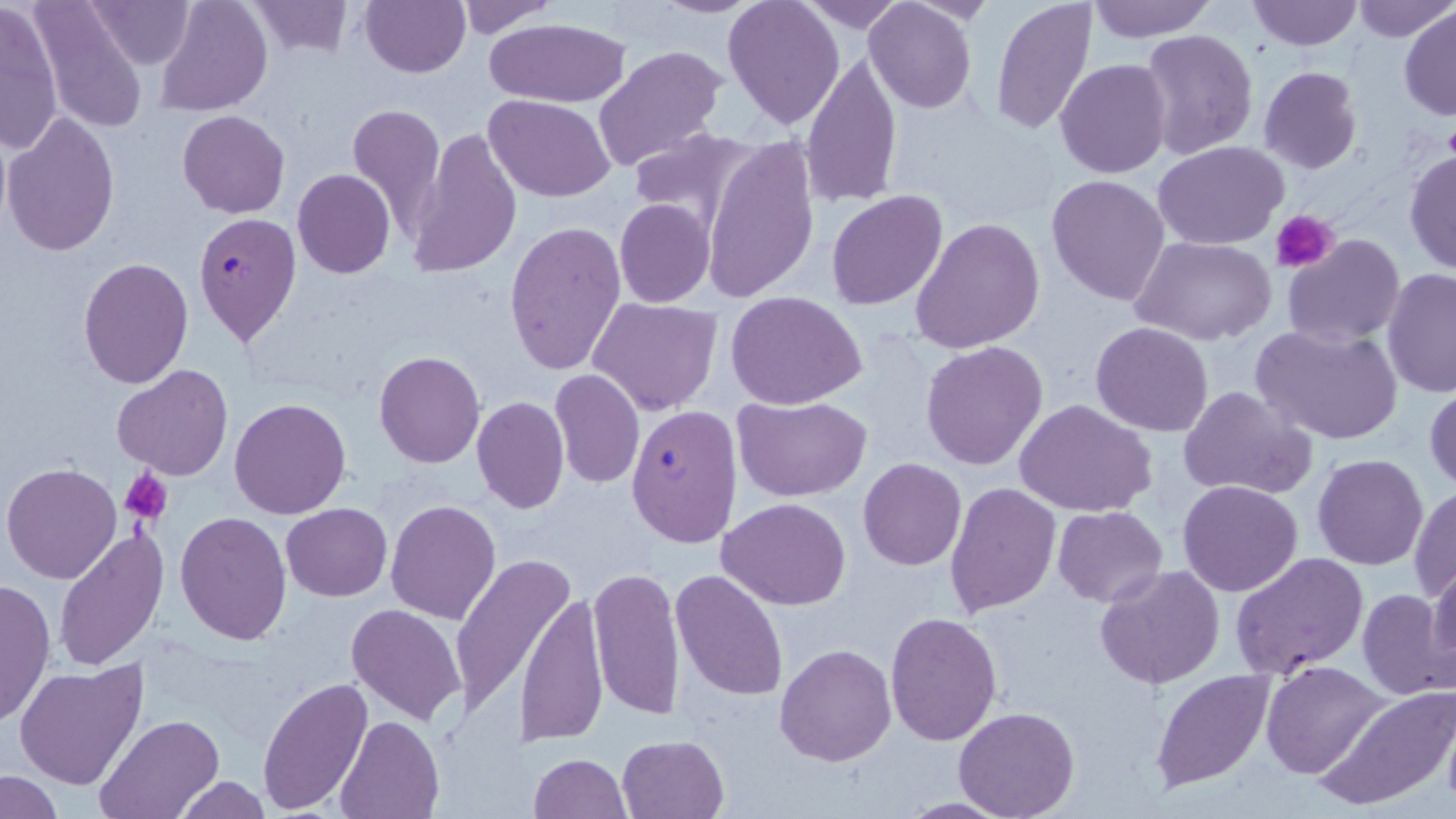

{
  "plasmodium_falciparum_infected_red_blood_cell_locations": "approximate bounding boxes as (x1, y1, x2, y2) in pixels: (195, 211, 302, 344), (625, 404, 742, 548)",
  "slide_level_diagnosis": "Plasmodium falciparum",
  "platelet_locations": "approximate bounding boxes as (x1, y1, x2, y2) in pixels: (1273, 210, 1340, 271), (120, 469, 172, 526)",
  "uninfected_red_blood_cell_locations": "approximate bounding boxes as (x1, y1, x2, y2) in pixels: (29, 0, 150, 135), (86, 0, 197, 70), (155, 0, 273, 117), (358, 0, 471, 78), (452, 0, 564, 37), (648, 0, 767, 18), (723, 0, 846, 129), (801, 0, 906, 33), (1247, 0, 1362, 50), (1350, 0, 1456, 43), (244, 1, 354, 59), (864, 1, 978, 113), (990, 1, 1098, 136), (1085, 1, 1218, 42), (0, 3, 64, 155), (1398, 5, 1455, 122), (483, 18, 632, 106), (1138, 29, 1258, 162), (593, 44, 727, 173), (799, 51, 903, 209), (1054, 58, 1171, 178), (1258, 67, 1363, 174), (486, 95, 615, 203), (347, 103, 446, 236), (177, 110, 290, 218), (2, 111, 122, 259), (628, 129, 763, 240), (407, 130, 524, 280), (701, 135, 820, 306), (1155, 140, 1288, 249), (323, 144, 429, 264), (1403, 148, 1456, 277), (292, 170, 396, 278), (1046, 174, 1171, 305), (826, 190, 947, 311), (614, 199, 713, 307), (911, 219, 1044, 354), (504, 220, 627, 375), (1281, 234, 1404, 348), (1130, 236, 1277, 348), (78, 259, 195, 388), (1381, 268, 1456, 397), (726, 292, 868, 410), (587, 298, 722, 417), (1090, 320, 1215, 436), (1250, 322, 1403, 446), (920, 340, 1049, 470), (373, 351, 485, 468), (113, 363, 233, 480), (549, 368, 645, 489), (1426, 384, 1456, 492), (1176, 385, 1319, 500), (732, 393, 871, 501), (471, 396, 569, 513), (229, 397, 351, 519), (1014, 400, 1158, 517), (1311, 453, 1429, 570), (858, 459, 967, 570), (3, 462, 122, 584), (945, 480, 1061, 617), (1178, 480, 1302, 597), (1408, 485, 1456, 600), (717, 497, 851, 610), (386, 499, 501, 624), (281, 503, 392, 601), (1052, 505, 1168, 606), (175, 512, 291, 647), (54, 529, 167, 672), (1230, 552, 1369, 679), (448, 554, 574, 719), (1427, 559, 1456, 677), (1093, 562, 1225, 690), (588, 565, 685, 722), (671, 569, 788, 700), (0, 579, 55, 727), (1356, 588, 1454, 702), (516, 589, 608, 747), (346, 602, 468, 726), (883, 609, 1002, 745), (774, 642, 897, 767), (1262, 655, 1388, 772), (14, 661, 149, 791), (1149, 669, 1276, 794), (258, 678, 375, 814), (1314, 683, 1456, 812), (952, 707, 1078, 819), (96, 715, 221, 819), (335, 715, 443, 818), (617, 733, 728, 818), (527, 753, 630, 818), (1, 771, 62, 818), (172, 776, 272, 818)",
  "magnification": "1000x",
  "modality": "light microscopy",
  "field_of_view": "one of a larger specimen",
  "stain": "May-Grünwald-Giemsa",
  "image_size": "1456×819 pixels",
  "preparation": "thin blood smear"
}